Locate every uninfected red blood cell.
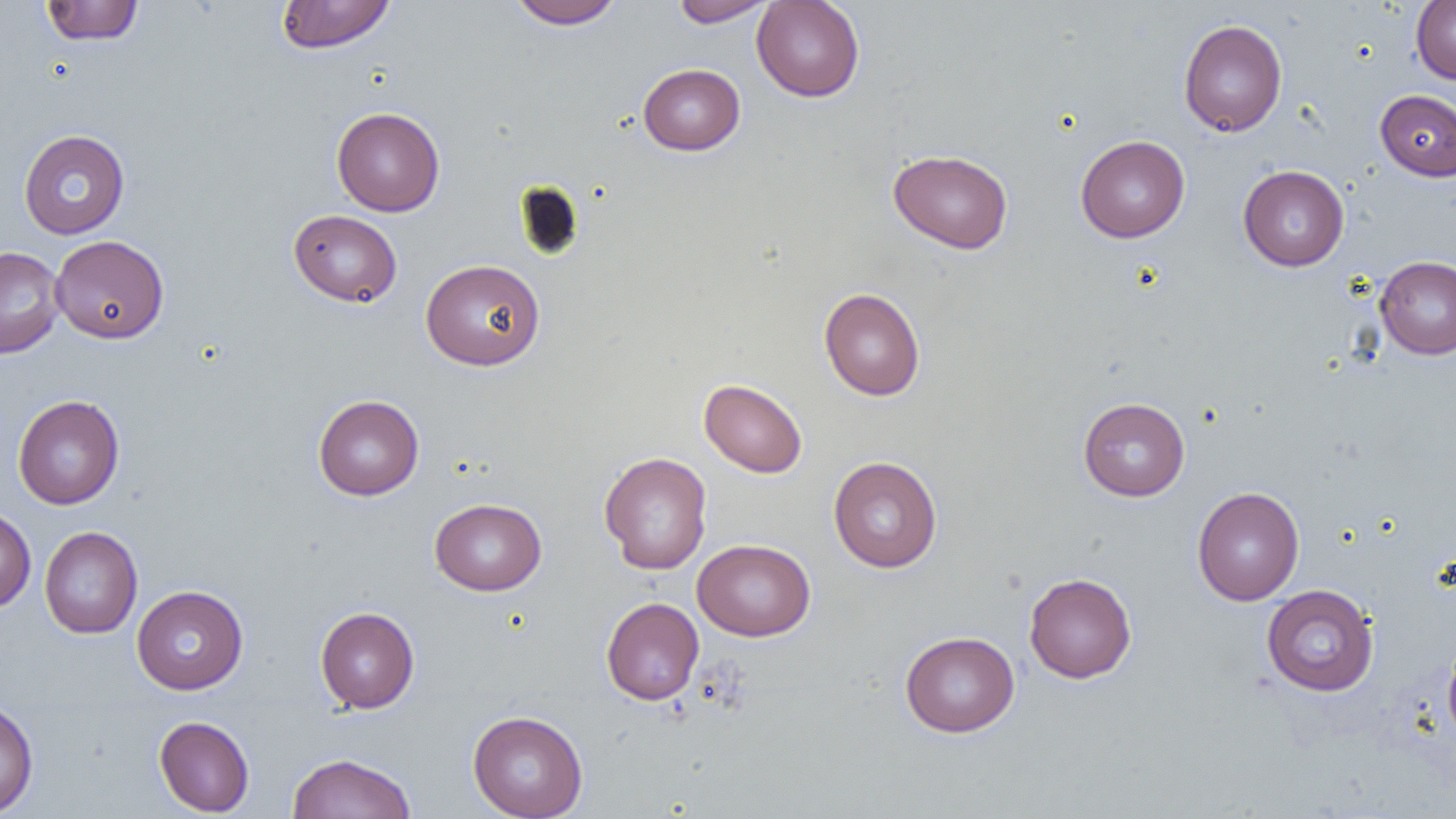
Approximate bounding boxes as [x1, y1, x2, y2] in pixels.
Uninfected red blood cells: [41, 0, 143, 46], [275, 0, 397, 54], [508, 0, 624, 30], [671, 0, 774, 27], [752, 0, 864, 102], [1411, 0, 1456, 84], [1178, 19, 1287, 136], [638, 64, 745, 155], [1375, 89, 1456, 181], [331, 106, 445, 216], [18, 129, 130, 239], [1075, 135, 1190, 242], [888, 149, 1013, 254], [1238, 165, 1349, 271], [288, 209, 402, 308], [50, 235, 168, 343], [0, 247, 65, 359], [1374, 255, 1456, 360], [421, 258, 545, 371], [819, 287, 925, 400], [699, 379, 808, 478], [13, 394, 124, 509], [313, 394, 424, 500], [1077, 397, 1190, 501], [599, 451, 712, 574], [828, 455, 943, 572], [1192, 486, 1304, 606], [429, 498, 547, 595], [0, 505, 36, 613], [40, 526, 143, 638], [692, 539, 815, 641], [1023, 572, 1136, 683], [1261, 584, 1380, 697], [132, 585, 248, 695], [601, 597, 704, 705], [315, 606, 419, 713], [900, 631, 1019, 737], [1442, 639, 1456, 747], [0, 698, 39, 818], [467, 710, 588, 818], [154, 715, 255, 816], [287, 753, 416, 818].

{
  "slide_level_diagnosis": "no evidence of blood parasites",
  "magnification": "1000x",
  "field_of_view": "one of a larger specimen",
  "preparation": "thin blood film",
  "modality": "optical microscopy",
  "image_size": "1456×819 pixels"
}